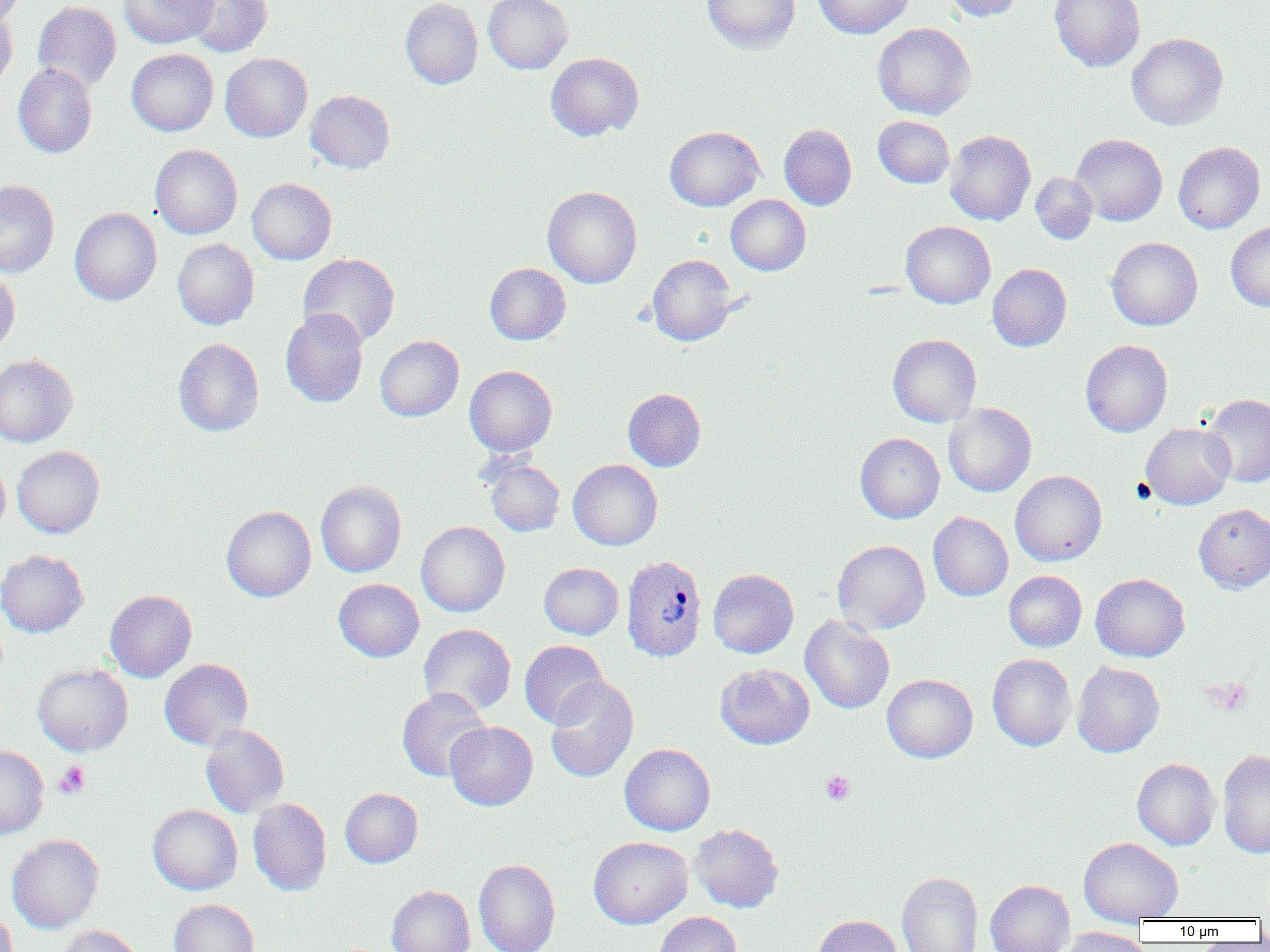

Approximate bounding boxes as (x1,y1)-(x2,y2) corner pairs in pixels. Platelet locations: (1209,677)-(1252,715), (54,761)-(90,799), (820,770)-(856,805). Plasmodium vivax-infected red blood cell locations: (621,555)-(707,662). Uninfected red blood cell locations: (0,0)-(26,28), (118,0)-(217,48), (183,0)-(272,57), (400,0)-(483,89), (483,0)-(573,73), (701,0)-(800,53), (814,0)-(913,39), (942,0)-(1024,22), (1049,0)-(1145,72), (33,1)-(121,92), (0,7)-(17,90), (872,22)-(976,120), (1126,33)-(1228,130), (126,49)-(218,136), (220,53)-(312,142), (545,53)-(643,141), (13,64)-(97,158), (305,90)-(395,173), (873,115)-(955,188), (779,124)-(857,210), (664,126)-(764,211), (945,130)-(1036,226), (1071,134)-(1167,226), (1173,142)-(1265,234), (150,144)-(242,239), (1030,172)-(1098,244), (247,178)-(336,265), (0,180)-(59,278), (542,186)-(642,288), (725,194)-(811,275), (70,207)-(161,306), (901,221)-(995,308), (1226,221)-(1270,312), (1106,237)-(1203,330), (172,239)-(259,330), (298,253)-(400,347), (647,254)-(739,346), (484,263)-(571,345), (987,263)-(1072,351), (0,268)-(20,358), (280,309)-(368,407), (888,334)-(981,427), (375,335)-(464,421), (173,338)-(264,437), (1080,340)-(1172,437), (0,354)-(78,447), (464,365)-(557,457), (623,388)-(706,471), (1201,393)-(1270,487), (943,403)-(1036,497), (1140,422)-(1236,510), (855,433)-(944,523), (12,446)-(104,538), (0,456)-(10,540), (485,459)-(564,536), (568,459)-(663,550), (1010,470)-(1107,566), (316,481)-(406,578), (1193,503)-(1270,593), (221,506)-(316,601), (928,512)-(1013,601), (416,521)-(509,617), (832,540)-(930,634), (0,550)-(89,637), (539,562)-(624,640), (708,569)-(798,658), (1004,571)-(1087,652), (1090,573)-(1190,662), (333,579)-(424,662), (105,590)-(197,682), (800,615)-(895,714), (418,624)-(516,716), (520,640)-(608,728), (987,654)-(1076,751), (159,659)-(253,750), (1072,661)-(1164,757), (715,663)-(815,749), (33,664)-(133,756), (882,674)-(978,762), (545,677)-(638,783), (397,688)-(491,781), (445,721)-(538,811), (200,724)-(289,817), (620,743)-(715,836), (0,745)-(49,839), (1217,749)-(1270,858), (1132,758)-(1220,850), (340,788)-(423,868), (248,798)-(331,896), (147,805)-(242,895), (689,824)-(784,912), (7,834)-(104,933), (588,837)-(692,929), (1078,837)-(1183,924), (473,858)-(561,952), (896,872)-(983,952), (985,880)-(1074,952), (386,885)-(475,952), (169,899)-(260,952), (0,907)-(18,952), (654,912)-(742,952), (812,914)-(902,952), (51,925)-(143,952), (1059,926)-(1150,952). Slide-level diagnosis: Plasmodium vivax. 1000x magnification. One field of a larger specimen. Thin blood smear. Image is 1270×952 pixels. Optical microscopy.